Comment on the morphology of the erythrocytes.
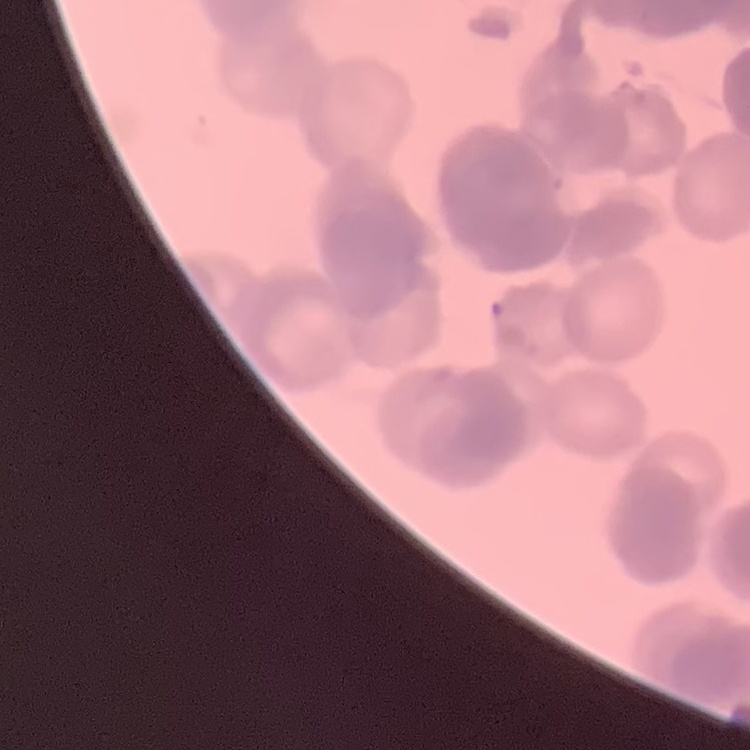

Rouleaux formation.

stain = Field's or Giemsa
image type = one tile cut from a larger photomicrograph
preparation = thin blood film